Assess the morphology of the erythrocytes.
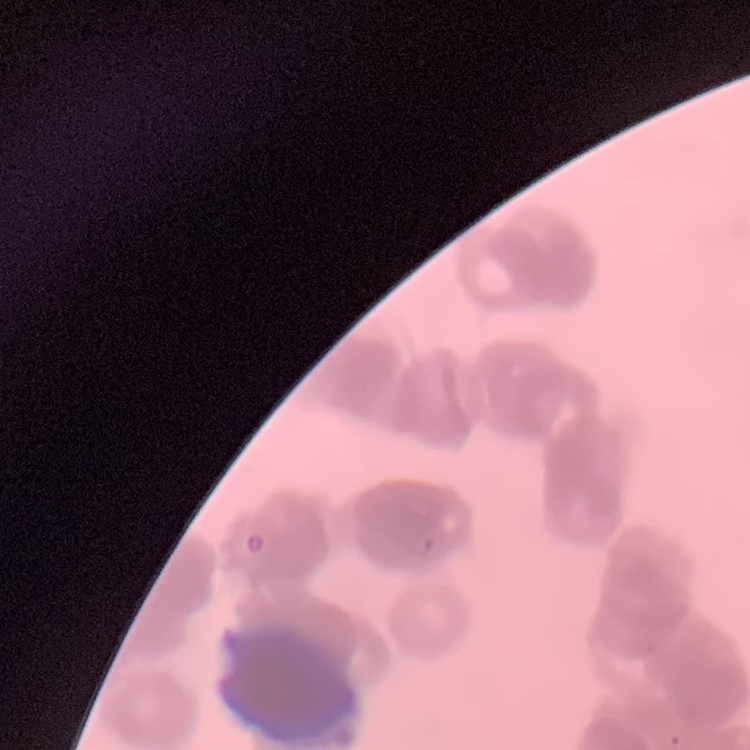
They show rouleaux formation.

preparation: thin blood film
image_type: one tile cut from a larger photomicrograph
stain: Field's or Giemsa